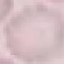

Result: no malaria parasites seen. Photographed with a smartphone camera at the microscope eyepiece. Thin blood film. Automatically extracted cell patch, resized to 64 × 64 pixels. Giemsa-stained preparation.